Describe the morphology of the erythrocytes.
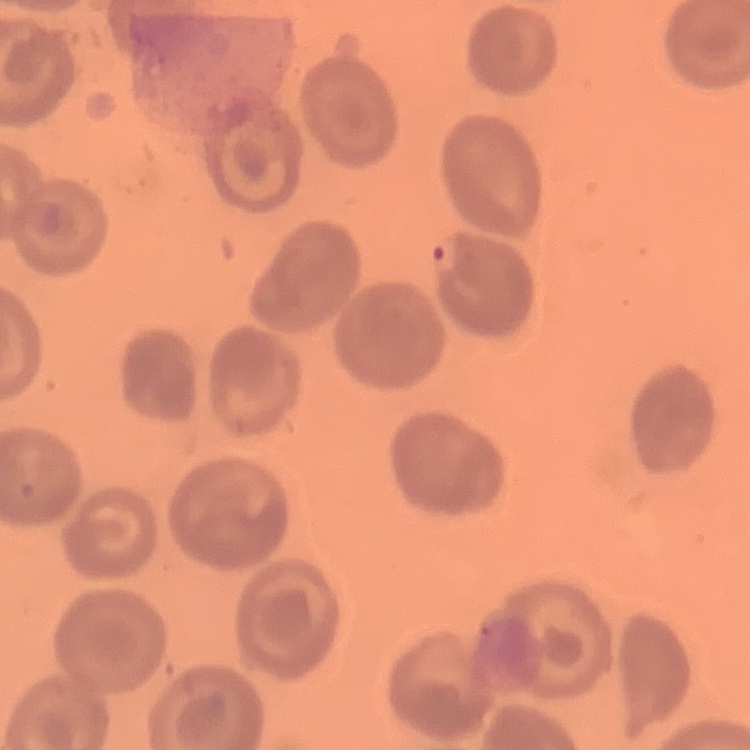
They show no rouleaux formation.

Summary:
  - Preparation: thin blood smear
  - Stain: Field's or Giemsa
  - Image type: one tile cut from a larger photomicrograph